Give the extent of all Plasmodium vivax-infected red blood cells.
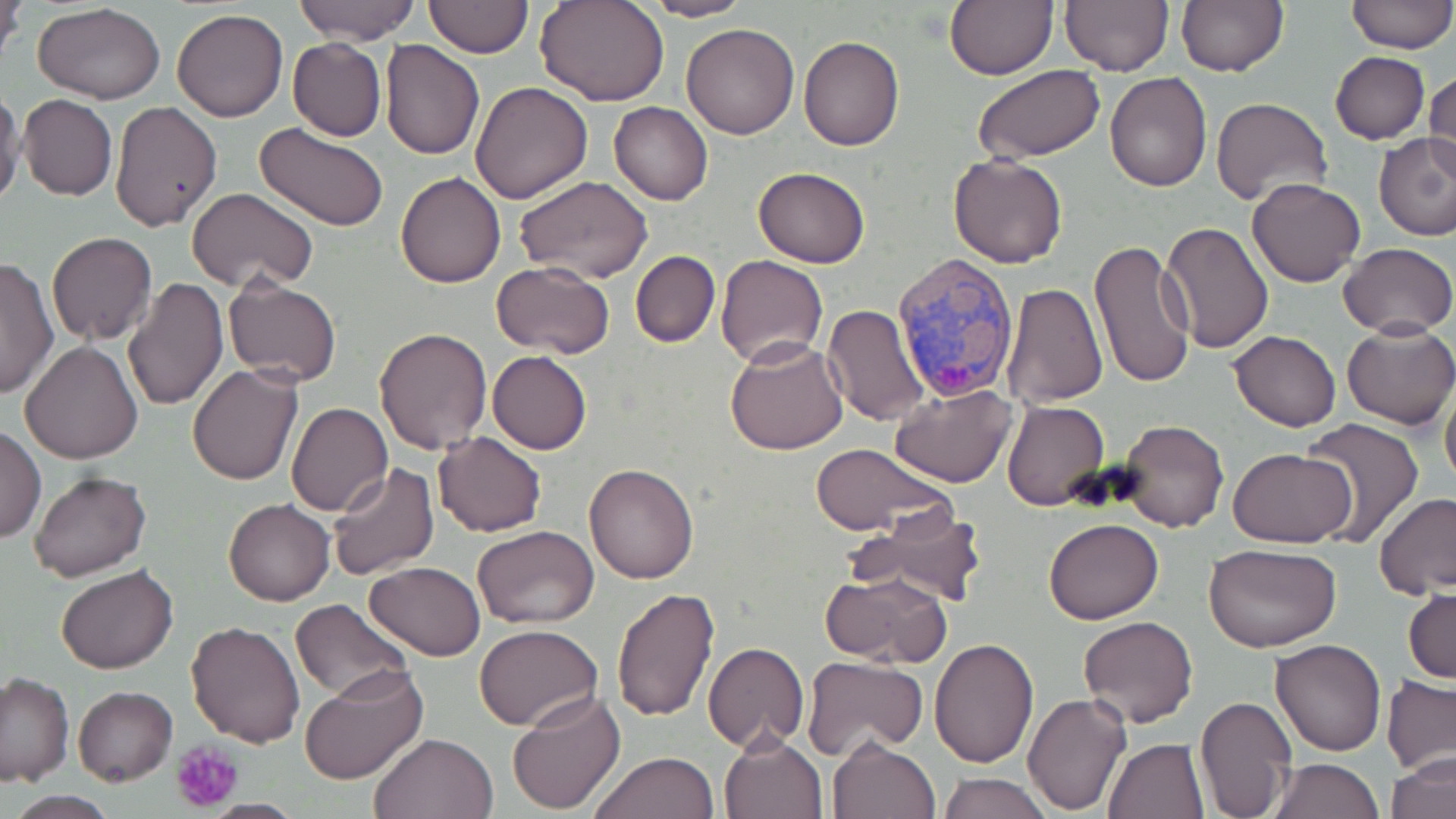

Approximate bounding boxes as (x1, y1, x2, y2) in pixels.
Plasmodium vivax-infected red blood cells: (892, 253, 1020, 402).

{
  "slide_level_diagnosis": "Plasmodium vivax",
  "preparation": "thin blood smear",
  "platelet_locations": "approximate bounding boxes as (x1, y1, x2, y2) in pixels: (171, 739, 245, 813)",
  "modality": "light microscopy",
  "uninfected_red_blood_cell_locations": "approximate bounding boxes as (x1, y1, x2, y2) in pixels: (293, 0, 419, 45), (537, 0, 670, 105), (642, 0, 753, 21), (944, 0, 1057, 80), (1060, 0, 1173, 76), (1175, 0, 1288, 76), (1346, 0, 1455, 54), (1, 1, 24, 74), (424, 1, 533, 57), (32, 3, 166, 104), (171, 8, 289, 122), (680, 22, 800, 139), (799, 36, 904, 151), (286, 37, 386, 141), (382, 40, 485, 160), (1330, 51, 1429, 144), (972, 64, 1103, 162), (1423, 68, 1455, 182), (1106, 71, 1212, 192), (470, 80, 595, 203), (0, 86, 24, 212), (18, 95, 117, 201), (1211, 97, 1333, 208), (110, 100, 223, 232), (608, 102, 712, 205), (255, 123, 388, 235), (1373, 132, 1456, 240), (948, 153, 1068, 268), (753, 166, 870, 267), (394, 172, 507, 289), (515, 174, 653, 284), (1246, 176, 1367, 288), (186, 188, 318, 295), (1159, 221, 1273, 356), (47, 232, 158, 344), (1091, 239, 1196, 389), (1337, 242, 1455, 339), (631, 251, 720, 347), (716, 254, 827, 368), (0, 255, 58, 399), (490, 261, 617, 359), (123, 278, 229, 413), (224, 278, 342, 387), (1001, 282, 1106, 406), (823, 303, 932, 426), (1342, 321, 1456, 429), (374, 326, 493, 454), (1228, 329, 1342, 431), (724, 338, 849, 456), (20, 340, 143, 464), (488, 351, 591, 454), (187, 363, 304, 484), (1440, 371, 1456, 497), (889, 382, 1017, 488), (1003, 401, 1109, 512), (286, 402, 393, 516), (1300, 418, 1426, 548), (1119, 420, 1228, 533), (1, 424, 45, 544), (433, 431, 546, 536), (809, 442, 953, 537), (1229, 446, 1357, 547), (326, 462, 440, 579), (584, 462, 700, 583), (28, 471, 153, 583), (1373, 492, 1456, 599), (222, 497, 334, 606), (855, 509, 987, 606), (1042, 518, 1164, 624), (473, 526, 599, 629), (1203, 541, 1344, 653), (364, 562, 485, 662), (57, 564, 178, 674), (821, 570, 950, 668), (1405, 586, 1455, 685), (611, 587, 720, 723), (290, 597, 412, 701), (1077, 615, 1198, 728), (186, 621, 307, 748), (474, 623, 602, 730), (1029, 636, 1156, 788), (929, 638, 1038, 768), (1269, 639, 1387, 757), (703, 643, 809, 752), (802, 655, 927, 760), (298, 666, 427, 786), (0, 672, 73, 787), (1381, 675, 1456, 776), (72, 687, 178, 786), (507, 691, 627, 815), (1022, 692, 1133, 816), (1196, 695, 1295, 817), (369, 731, 498, 818), (719, 733, 829, 819), (826, 738, 941, 819), (1102, 738, 1211, 819), (1387, 750, 1456, 819), (589, 752, 718, 819), (1269, 758, 1382, 819), (939, 773, 1054, 819), (6, 793, 118, 819)",
  "stain": "May-Grünwald-Giemsa",
  "image_size": "1456×819 pixels",
  "field_of_view": "one of a larger specimen",
  "magnification": "1000x"
}